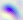 Toxoplasma gondii is seen. Micrograph. Captured at 400x magnification.